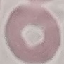

Summary:
  - Result: no malaria parasites detected
  - Capture: smartphone camera at the microscope eyepiece
  - Preparation: thin blood smear
  - Stain: Giemsa
  - Image type: automatically extracted cell patch, resized to 64 × 64 pixels